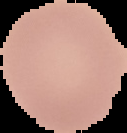
Summary:
  - Result: no Plasmodium parasites seen
  - Image size: 127×133 pixels
  - Image type: segmented cell region with the area outside set to black
  - Preparation: thin blood smear